Identify the parasite.
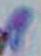
Toxoplasma gondii.

Summary:
  - Magnification: 1000x
  - Modality: micrograph